Comment on the morphology of the red blood cells.
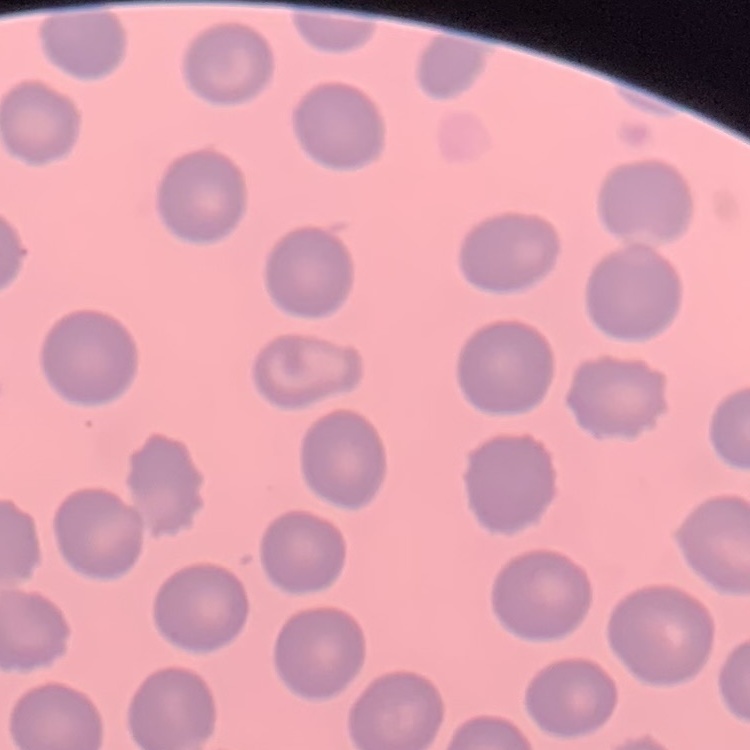
They show no rouleaux formation.

Thin blood film. Stained with either Field's or Giemsa. One tile cut from a larger photomicrograph.